Locate leukocytes (white blood cells).
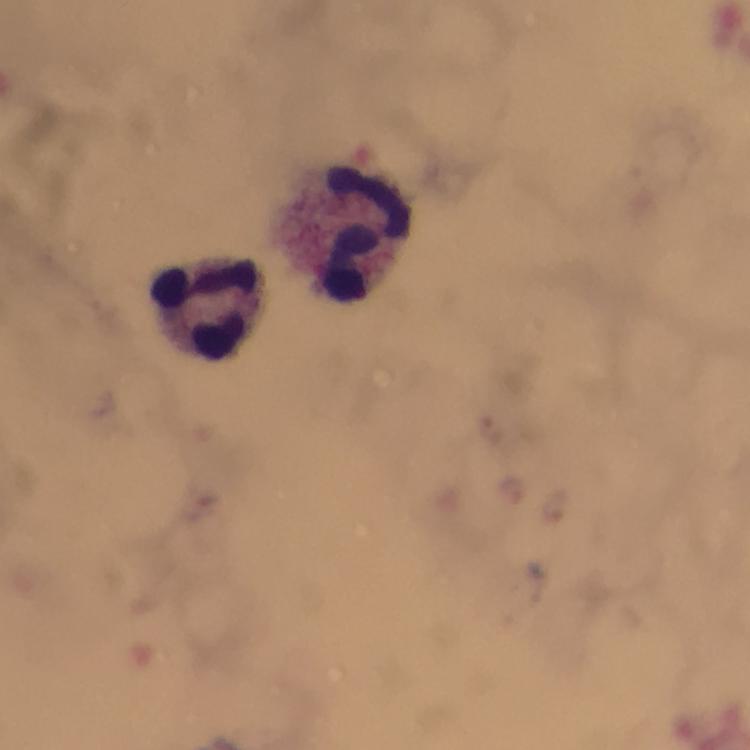

Approximate centers as (x, y) in pixels.
Leukocytes: (352, 233), (211, 312).

Plasmodium parasite locations: (494, 430), (513, 493), (552, 505). Cropped region of a single field of view. Image is 750×750 pixels. From a diagnostic examination for malaria. Thick blood film. Giemsa stain. At 100x magnification. Smartphone photograph taken through a microscope. Immersion oil applied.